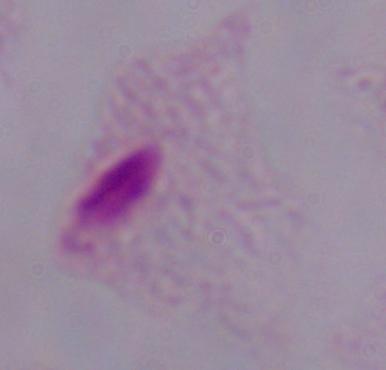

magnification: 1000x
identification: trichomonad
modality: micrograph